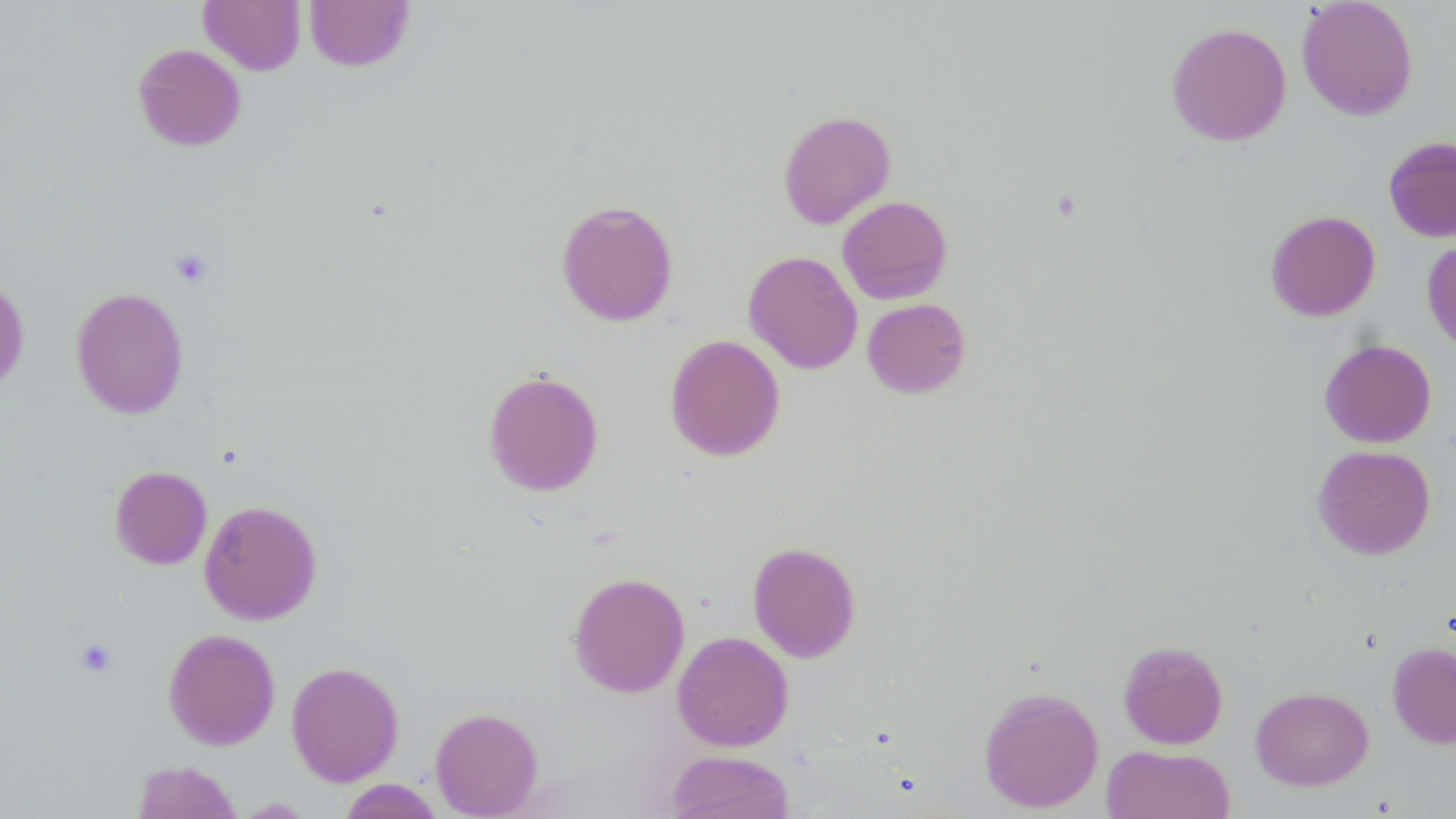

slide-level diagnosis = no evidence of blood parasites
magnification = 1000x
stain = May-Grünwald-Giemsa
image size = 1456×819 pixels
uninfected red blood cell locations = approximate bounding boxes as (x1, y1, x2, y2) in pixels: (304, 0, 415, 72), (1296, 0, 1419, 121), (199, 1, 306, 75), (1166, 22, 1292, 146), (132, 43, 246, 151), (777, 110, 896, 229), (1383, 135, 1456, 242), (837, 195, 953, 305), (556, 199, 679, 327), (1264, 210, 1381, 321), (1422, 238, 1456, 356), (743, 250, 863, 374), (0, 274, 30, 395), (70, 286, 190, 420), (862, 298, 972, 398), (664, 333, 785, 461), (1318, 339, 1437, 448), (482, 369, 604, 497), (1312, 445, 1436, 559), (109, 465, 212, 570), (199, 499, 323, 625), (747, 541, 861, 663), (568, 572, 690, 698), (163, 629, 280, 750), (672, 631, 794, 751), (1118, 640, 1229, 749), (1387, 641, 1456, 749), (286, 661, 404, 786), (978, 685, 1104, 813), (1250, 686, 1374, 791), (430, 707, 543, 818), (1100, 745, 1235, 819), (665, 750, 795, 819), (131, 760, 243, 818), (338, 779, 444, 819)
platelet locations = approximate bounding boxes as (x1, y1, x2, y2) in pixels: (170, 249, 214, 288), (75, 638, 118, 678)
modality = light microscopy
preparation = thin blood smear
field of view = single